Assess this cell for malaria.
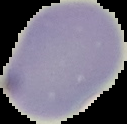
It is uninfected.

Summary:
  - Preparation: thin blood smear
  - Image size: 127×124 pixels
  - Image type: cell region segmented out of the field of view; surrounding area masked to black